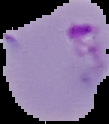

result = malaria parasites detected
image size = 109×124 pixels
preparation = thin blood film
image type = segmented cell region on a black background